Classify this cell by malaria status.
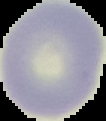

It is uninfected.

image size = 106×121 pixels
image type = segmented cell region on a black background
preparation = thin blood film